Assess this cell for malaria.
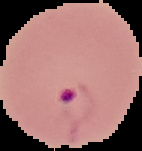

Parasitized.

{
  "image_type": "cell region segmented out of the field of view; surrounding area masked to black",
  "image_size": "142×151 pixels",
  "preparation": "thin blood smear"
}